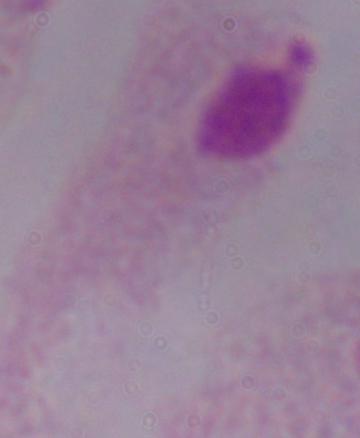 Captured at 1000x magnification. A trichomonad is seen. Micrograph.